Locate and identify every blood parasite.
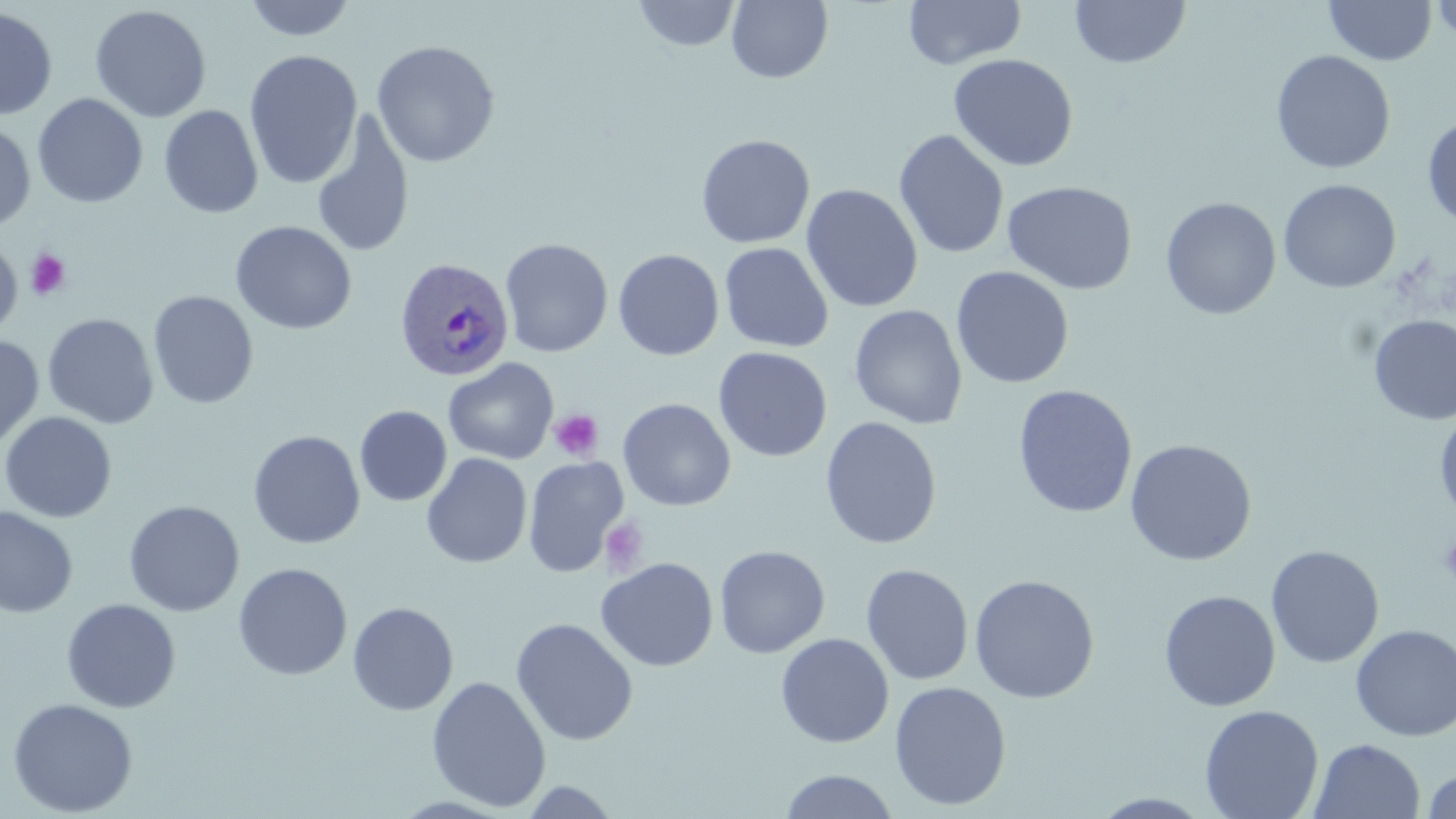

Approximate bounding boxes as (x1, y1, x2, y2) in pixels.
Plasmodium ovale-infected red blood cells: (392, 258, 512, 383).
No Plasmodium falciparum, Plasmodium malariae, Plasmodium vivax, Babesia divergens, or Trypanosoma brucei observed.

slide-level diagnosis = Plasmodium ovale
modality = optical microscopy
image size = 1456×819 pixels
field of view = one of a larger specimen
preparation = thin blood smear
magnification = 1000x
platelet locations = approximate bounding boxes as (x1, y1, x2, y2) in pixels: (26, 248, 72, 300), (549, 410, 604, 461), (599, 517, 650, 576), (1438, 534, 1456, 588)
stain = May-Grünwald-Giemsa
uninfected red blood cell locations = approximate bounding boxes as (x1, y1, x2, y2) in pixels: (242, 0, 359, 42), (726, 0, 833, 84), (903, 0, 1026, 70), (1069, 0, 1192, 69), (1324, 0, 1437, 66), (1431, 0, 1456, 45), (632, 1, 741, 52), (89, 4, 212, 123), (0, 7, 58, 120), (371, 40, 500, 168), (244, 50, 363, 190), (1271, 50, 1395, 174), (948, 53, 1079, 172), (32, 93, 148, 209), (159, 105, 264, 219), (311, 109, 415, 260), (1422, 116, 1456, 230), (0, 120, 36, 232), (893, 129, 1010, 260), (696, 134, 815, 249), (1278, 178, 1401, 294), (1002, 181, 1138, 295), (801, 183, 923, 313), (1160, 196, 1281, 320), (230, 220, 357, 335), (0, 236, 22, 339), (500, 238, 614, 358), (719, 242, 833, 353), (613, 249, 725, 361), (951, 266, 1074, 389), (148, 290, 259, 409), (849, 304, 968, 429), (43, 313, 158, 429), (1369, 315, 1456, 425), (0, 335, 44, 454), (713, 346, 832, 463), (444, 358, 558, 464), (1012, 384, 1139, 518), (617, 397, 736, 511), (355, 406, 452, 507), (1434, 407, 1456, 525), (0, 412, 118, 524), (820, 416, 942, 550), (247, 429, 366, 550), (1124, 439, 1257, 566), (422, 453, 532, 569), (523, 456, 629, 578), (123, 500, 245, 617), (0, 506, 78, 618), (714, 545, 830, 658), (1265, 545, 1384, 668), (595, 557, 718, 672), (233, 562, 353, 681), (860, 563, 974, 686), (968, 574, 1100, 704), (1158, 589, 1281, 712), (61, 599, 181, 713), (347, 602, 459, 716), (511, 618, 638, 746), (1350, 624, 1456, 742), (775, 633, 894, 748), (426, 675, 552, 812), (889, 681, 1012, 811), (6, 698, 139, 817), (1199, 704, 1324, 819), (1309, 738, 1426, 819), (1421, 767, 1456, 818), (778, 769, 901, 818), (516, 779, 625, 818), (1088, 792, 1216, 817)